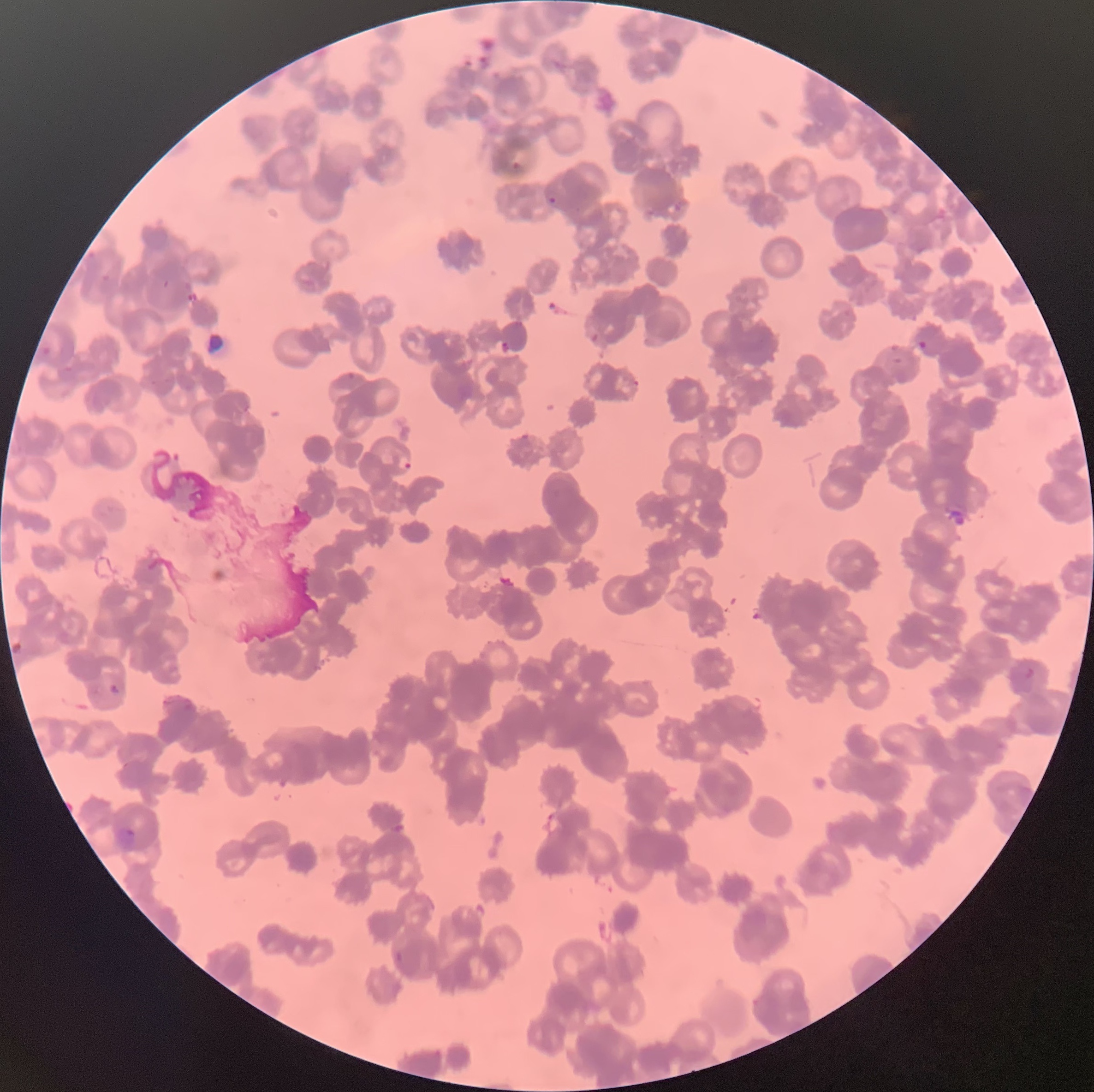

Approximate bounding boxes as (x1, y1, x2, y2) in pixels. Plasmodium parasite locations: (505, 161, 522, 173), (548, 196, 557, 205), (501, 339, 511, 353), (918, 340, 927, 351), (632, 378, 640, 388), (398, 454, 413, 473), (10, 636, 23, 655), (1010, 666, 1035, 695), (105, 679, 119, 694), (546, 811, 563, 833), (113, 825, 137, 853), (395, 948, 406, 965). Thin blood smear. Light microscopy. The red blood cells show rouleaux formation. Image is 1094×1092 pixels.